Name the blood parasite species.
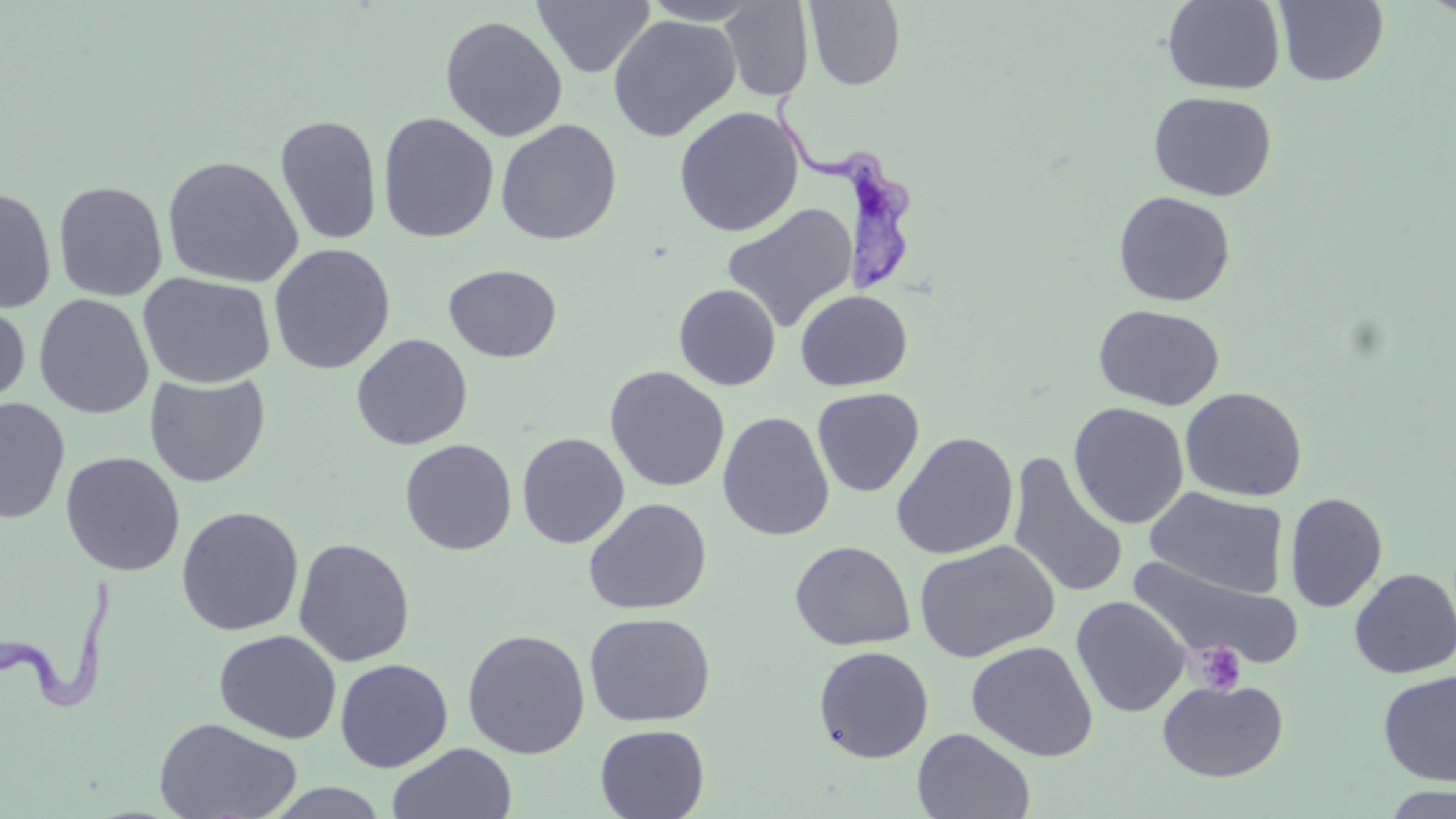
Trypanosoma brucei.

image_size: 1456×819 pixels
modality: light microscopy
uninfected_red_blood_cell_locations: 'approximate bounding boxes as (x1, y1, x2, y2) in pixels: (532, 0, 655, 79), (639, 0, 765, 25), (1163, 0, 1286, 95), (719, 1, 815, 102), (804, 1, 906, 91), (1273, 1, 1390, 86), (607, 14, 741, 142), (440, 15, 568, 142), (1148, 91, 1278, 201), (674, 106, 805, 237), (377, 112, 499, 243), (274, 114, 383, 246), (494, 118, 622, 246), (162, 154, 303, 288), (52, 180, 169, 302), (0, 186, 57, 314), (1113, 190, 1236, 306), (721, 203, 858, 332), (268, 243, 396, 375), (443, 263, 562, 363), (137, 272, 276, 390), (673, 283, 781, 391), (794, 289, 913, 391), (33, 293, 154, 420), (0, 299, 31, 416), (1093, 304, 1225, 411), (351, 333, 473, 451), (604, 365, 730, 492), (144, 372, 271, 488), (1180, 386, 1307, 501), (811, 387, 925, 497), (0, 397, 70, 525), (1068, 402, 1189, 529), (717, 411, 835, 541), (516, 432, 630, 549), (891, 432, 1018, 560), (399, 438, 518, 555), (60, 452, 186, 577), (1007, 452, 1128, 601), (1146, 487, 1289, 598), (1285, 492, 1388, 612), (583, 497, 712, 615), (175, 506, 304, 636), (293, 537, 416, 667), (914, 540, 1060, 662), (789, 541, 915, 651), (1128, 556, 1304, 672), (1349, 568, 1456, 679), (1071, 596, 1190, 717), (583, 612, 716, 727), (462, 628, 590, 759), (214, 629, 341, 743), (966, 641, 1098, 761), (813, 645, 934, 763), (334, 658, 453, 772), (1377, 670, 1456, 786), (1157, 678, 1288, 783), (153, 717, 304, 819), (594, 724, 710, 818), (912, 728, 1035, 818), (387, 742, 518, 819), (263, 782, 391, 818), (1379, 785, 1456, 819)'
trypanosoma_brucei_locations: 'approximate bounding boxes as (x1, y1, x2, y2) in pixels: (761, 84, 920, 296), (0, 573, 127, 716)'
magnification: 1000x
preparation: thin blood smear
platelet_locations: 'approximate bounding boxes as (x1, y1, x2, y2) in pixels: (1194, 641, 1245, 695)'
stain: May-Grünwald-Giemsa
field_of_view: one of a larger specimen